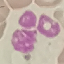
{
  "malaria_status": "uninfected",
  "stain": "Giemsa",
  "image_type": "cell patch, automatically extracted from a larger field of view and resized to 64 × 64 pixels",
  "capture": "smartphone through the microscope eyepiece",
  "preparation": "thin blood smear"
}